Identify the cell.
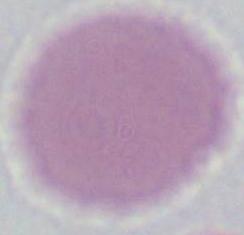

This is an erythrocyte.

Summary:
  - Modality: micrograph
  - Magnification: 1000x